Identify the cell.
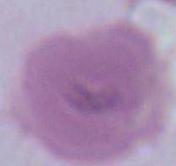
This is an erythrocyte.

Micrograph. Captured at 1000x magnification.